Assess for malaria.
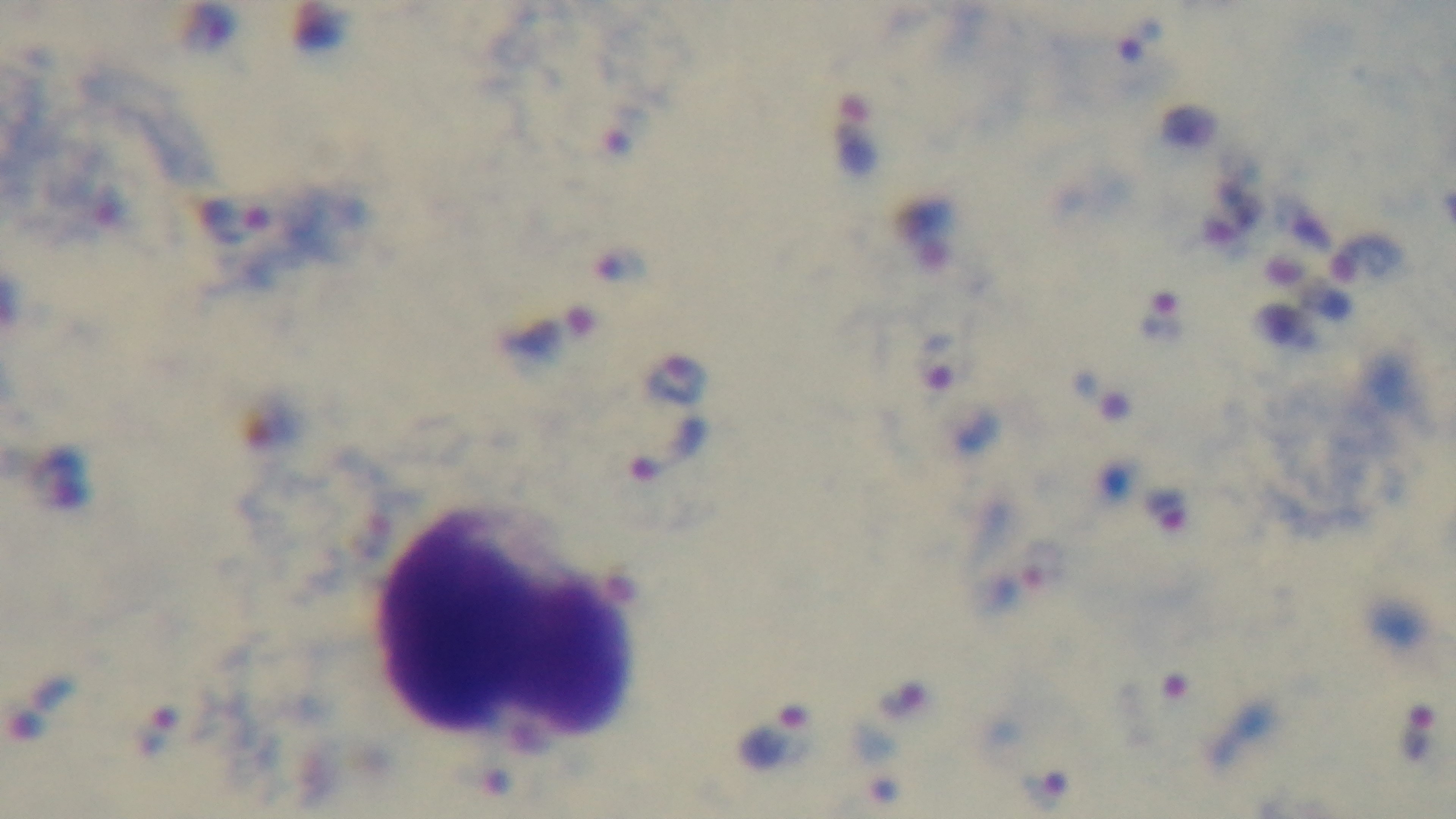

It is infected.

Oil-immersion objective, 100x. Giemsa-stained. Mounted 4K digital camera. Preparation: thick smear. Single field of view. Light microscopy.